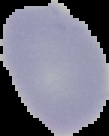
The area outside the segmented cell region is set to black. Image is 109×136 pixels. From a thin blood film. Malaria status: uninfected.